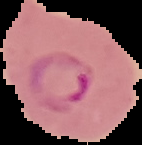

result: malaria parasites detected
image_type: cell region segmented out of the field of view; surrounding area masked to black
preparation: thin blood film
image_size: 142×145 pixels